Comment on the morphology of the red blood cells.
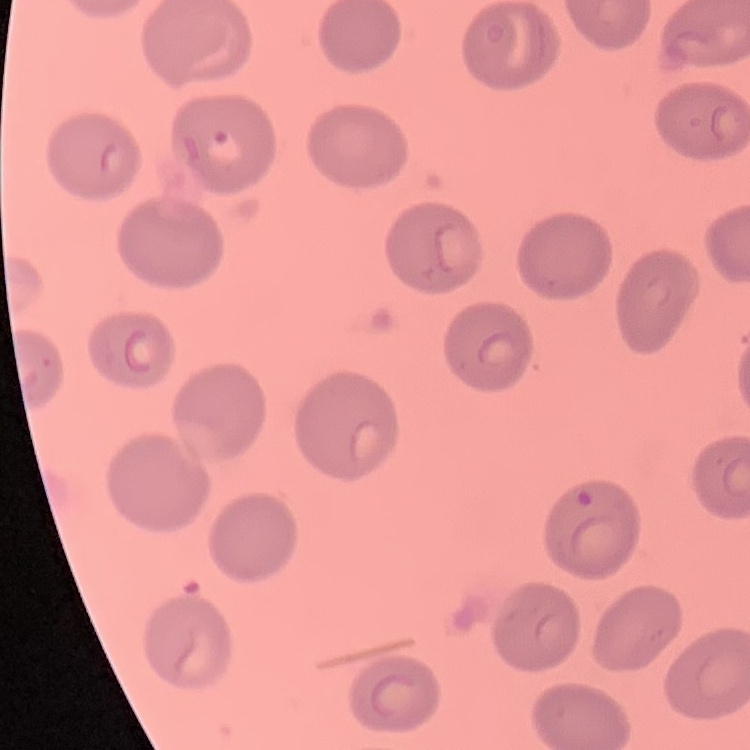

They show no rouleaux formation.

Field's or Giemsa stain. One tile cut from a larger photomicrograph. Thin blood smear.